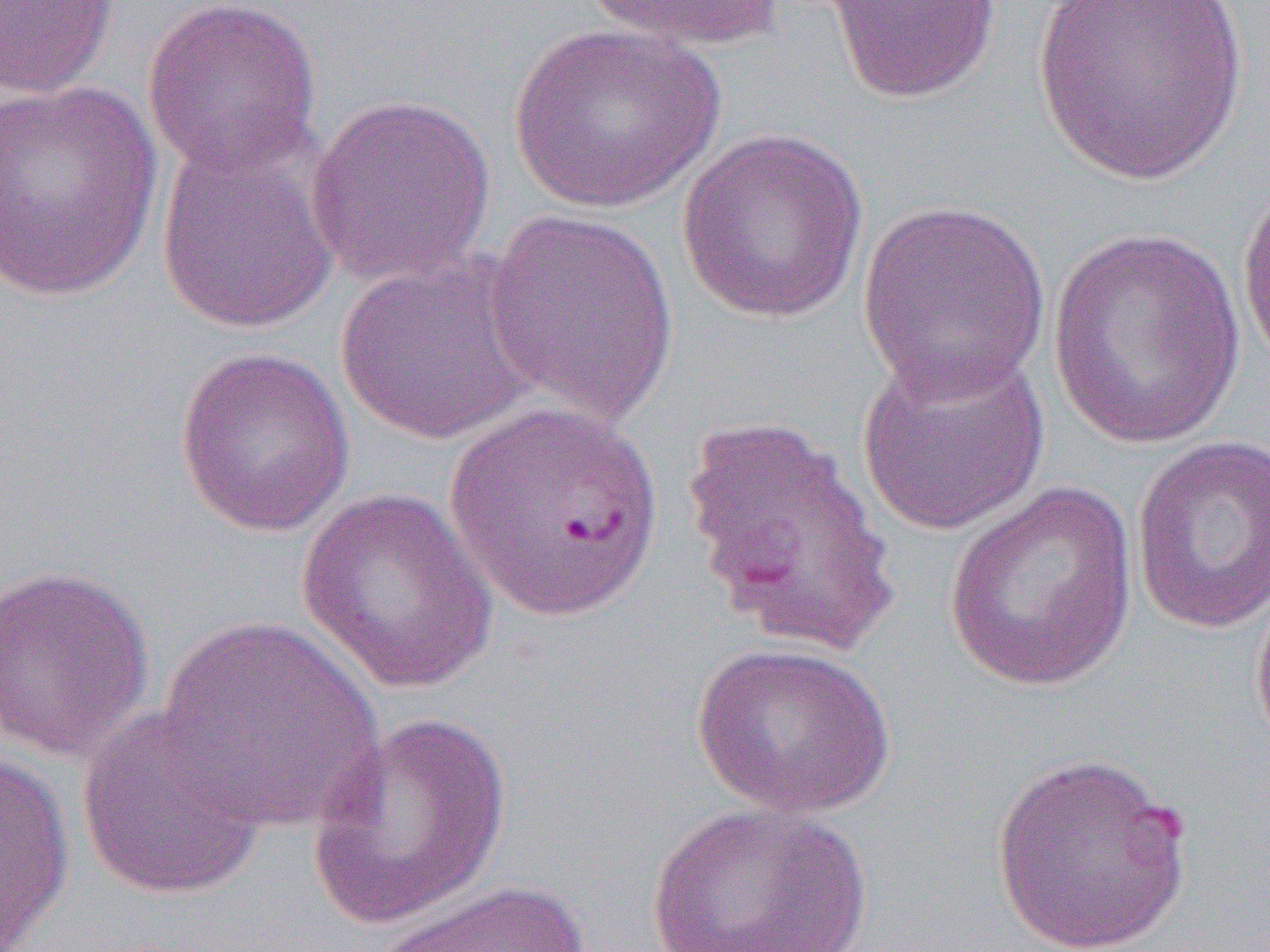 Approximate bounding boxes as (x1, y1, x2, y2) in pixels. Uninfected red blood cell locations: (0, 0, 119, 98), (141, 0, 323, 178), (578, 0, 791, 54), (822, 0, 1005, 105), (1033, 0, 1249, 186), (506, 22, 726, 214), (0, 79, 163, 303), (306, 93, 496, 289), (676, 129, 870, 325), (154, 132, 341, 336), (1235, 168, 1270, 372), (856, 197, 1054, 402), (482, 209, 680, 427), (1045, 223, 1252, 450), (334, 250, 545, 447), (855, 342, 1053, 537), (174, 345, 356, 537), (679, 412, 902, 658), (1130, 434, 1270, 634), (943, 483, 1140, 692), (295, 490, 500, 695), (1, 563, 157, 763), (1249, 577, 1270, 765), (154, 617, 385, 832), (690, 640, 897, 819), (75, 707, 269, 902), (306, 712, 514, 931), (0, 746, 75, 949), (990, 749, 1195, 952), (644, 802, 872, 952), (366, 880, 595, 952). Slide-level diagnosis: Plasmodium falciparum. 1000x magnification. Optical microscopy. Image is 1270×952 pixels. One field of a larger specimen. Thin blood smear.